Describe the morphology of the red blood cells.
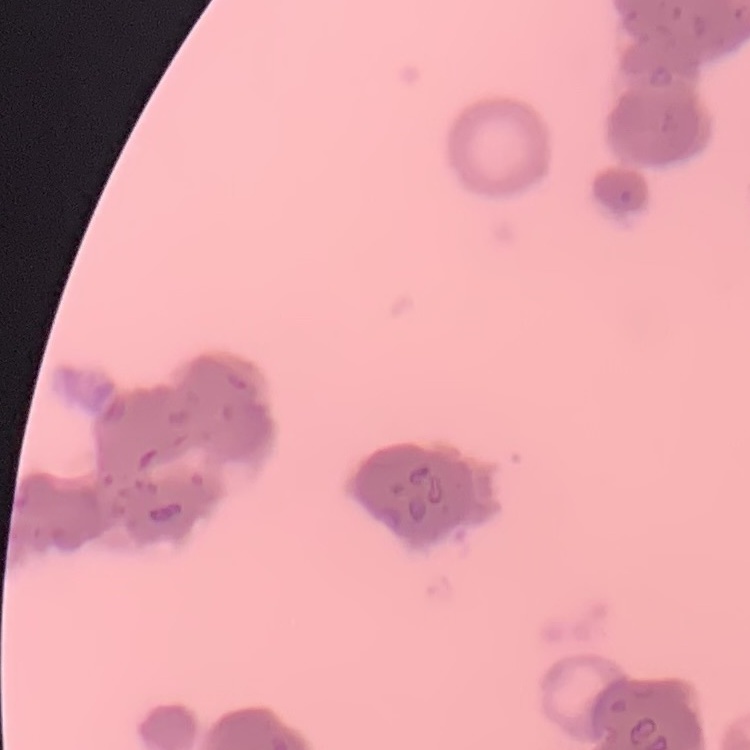
Rouleaux formation.

Field's or Giemsa stain. Square crop of a larger photomicrograph. Thin blood film.